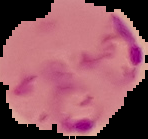

Result: malaria parasites detected. The area outside the segmented cell region is set to black. From a thin blood film. Image is 148×139 pixels.